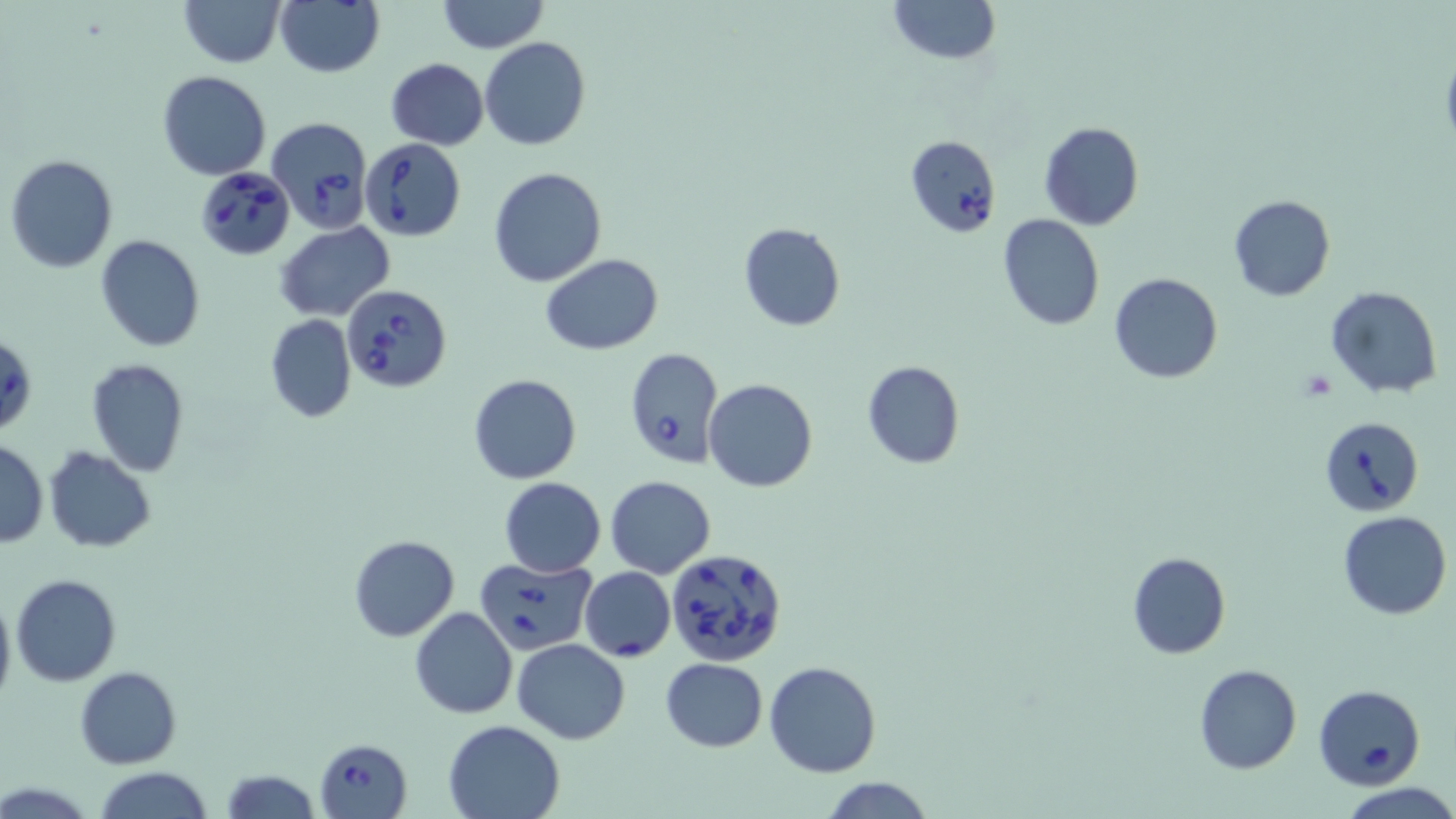
Summary:
  - Coordinate format: approximate bounding boxes as [x1, y1, x2, y2] in pixels
  - Babesia divergens-infected red blood cell locations: [264, 117, 371, 234], [361, 138, 466, 241], [195, 165, 296, 259], [341, 285, 452, 394], [624, 347, 724, 468], [1320, 417, 1423, 516], [666, 547, 790, 667], [473, 556, 596, 654], [579, 567, 676, 661], [1313, 684, 1426, 790], [313, 737, 412, 819]
  - Uninfected red blood cell locations: [178, 0, 286, 67], [275, 0, 384, 77], [435, 0, 551, 53], [886, 0, 999, 65], [480, 37, 590, 150], [385, 59, 488, 150], [157, 70, 270, 180], [1040, 121, 1144, 230], [905, 135, 1000, 238], [5, 155, 119, 273], [487, 166, 607, 288], [1228, 194, 1334, 301], [997, 215, 1104, 330], [275, 222, 395, 320], [738, 223, 846, 332], [96, 235, 205, 352], [541, 253, 662, 354], [1110, 273, 1222, 384], [1326, 286, 1441, 398], [265, 314, 357, 423], [1, 333, 37, 437], [85, 359, 191, 476], [862, 360, 964, 470], [467, 374, 583, 484], [704, 378, 817, 493], [0, 440, 47, 548], [44, 448, 156, 553], [605, 475, 715, 578], [499, 477, 606, 576], [1338, 510, 1452, 620], [350, 535, 459, 641], [1127, 553, 1232, 659], [11, 575, 121, 687], [0, 590, 15, 708], [410, 606, 517, 719], [512, 638, 630, 745], [660, 657, 768, 751], [764, 660, 881, 778], [1194, 664, 1301, 774], [75, 666, 182, 768], [443, 719, 567, 818], [93, 767, 215, 819], [221, 768, 319, 819], [819, 778, 937, 817], [1340, 783, 1456, 819]
  - Slide-level diagnosis: Babesia divergens
  - Image size: 1456×819 pixels
  - Modality: light microscopy
  - Magnification: 1000x
  - Stain: May-Grünwald-Giemsa
  - Preparation: thin blood smear
  - Field of view: one of a larger specimen